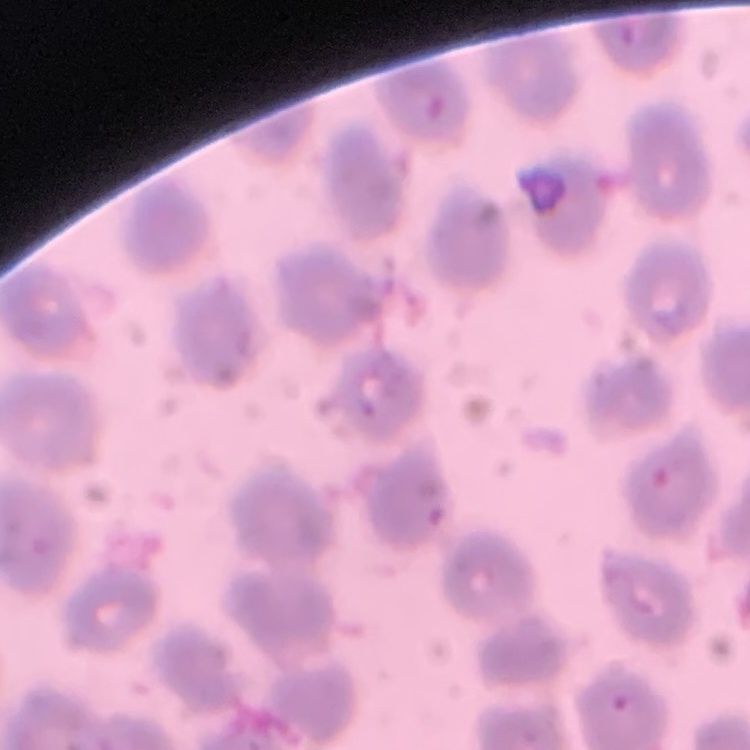

The erythrocytes exhibit no rouleaux formation. Square crop of a larger photomicrograph. Thin blood smear. Stained with either Field's or Giemsa.